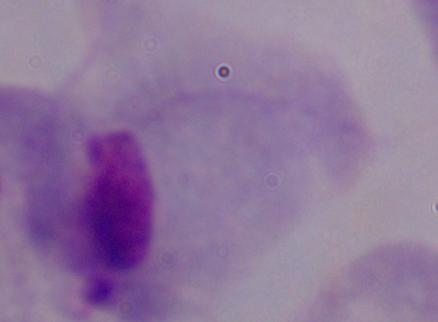

1000x magnification. Micrograph. A trichomonad is seen.